Name the parasite shown.
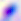
Toxoplasma gondii.

{
  "modality": "photomicrograph",
  "magnification": "400x"
}